State which cell type is depicted.
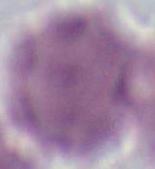
An erythrocyte.

Captured at 1000x magnification. Micrograph.